Locate and identify every blood parasite.
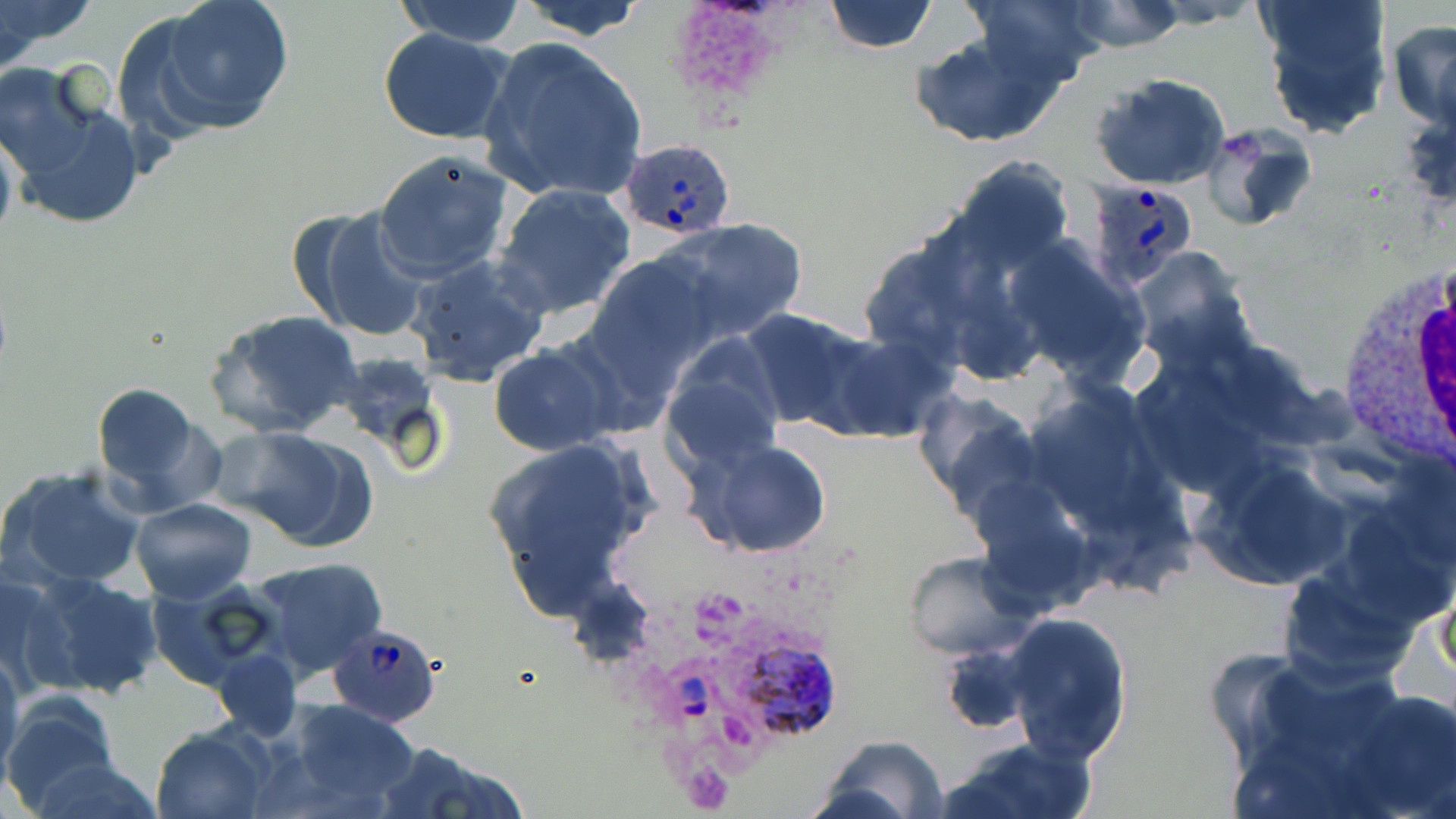

Approximate bounding boxes as named x1/y1/x2/y2 corners in pixels.
Plasmodium ovale-infected red blood cells: (x1=620, y1=135, x2=736, y2=240), (x1=1085, y1=178, x2=1198, y2=290), (x1=328, y1=622, x2=441, y2=727), (x1=660, y1=630, x2=835, y2=737).
No Plasmodium falciparum, Plasmodium malariae, Plasmodium vivax, Babesia divergens, or Trypanosoma brucei observed.

Platelet locations: (x1=664, y1=0, x2=795, y2=108). Uninfected red blood cell locations: (x1=0, y1=0, x2=99, y2=66), (x1=391, y1=0, x2=530, y2=47), (x1=513, y1=0, x2=650, y2=40), (x1=821, y1=0, x2=938, y2=54), (x1=966, y1=0, x2=1106, y2=90), (x1=1145, y1=0, x2=1262, y2=27), (x1=1256, y1=0, x2=1396, y2=139), (x1=140, y1=1, x2=296, y2=136), (x1=1065, y1=2, x2=1186, y2=52), (x1=1389, y1=17, x2=1456, y2=128), (x1=376, y1=29, x2=516, y2=145), (x1=910, y1=29, x2=1066, y2=149), (x1=477, y1=36, x2=649, y2=208), (x1=2, y1=67, x2=144, y2=228), (x1=1092, y1=71, x2=1232, y2=190), (x1=1201, y1=122, x2=1318, y2=231), (x1=0, y1=124, x2=18, y2=254), (x1=374, y1=147, x2=514, y2=282), (x1=949, y1=157, x2=1073, y2=275), (x1=490, y1=183, x2=638, y2=320), (x1=297, y1=205, x2=434, y2=344), (x1=655, y1=217, x2=807, y2=344), (x1=1004, y1=236, x2=1149, y2=383), (x1=1129, y1=245, x2=1255, y2=370), (x1=587, y1=250, x2=725, y2=381), (x1=404, y1=255, x2=550, y2=386), (x1=737, y1=307, x2=881, y2=434), (x1=204, y1=308, x2=365, y2=440), (x1=660, y1=336, x2=785, y2=475), (x1=487, y1=344, x2=623, y2=456), (x1=90, y1=381, x2=211, y2=505), (x1=1023, y1=383, x2=1169, y2=532), (x1=913, y1=390, x2=1043, y2=523), (x1=209, y1=427, x2=364, y2=544), (x1=480, y1=438, x2=656, y2=618), (x1=693, y1=439, x2=834, y2=559), (x1=1201, y1=457, x2=1350, y2=590), (x1=2, y1=464, x2=147, y2=591), (x1=130, y1=498, x2=258, y2=604), (x1=903, y1=552, x2=1029, y2=659), (x1=246, y1=557, x2=388, y2=680), (x1=0, y1=567, x2=94, y2=698), (x1=24, y1=572, x2=164, y2=699), (x1=145, y1=580, x2=285, y2=688), (x1=1432, y1=582, x2=1455, y2=678), (x1=1001, y1=613, x2=1132, y2=763), (x1=0, y1=646, x2=23, y2=784), (x1=214, y1=649, x2=300, y2=742), (x1=1221, y1=659, x2=1433, y2=819), (x1=1339, y1=687, x2=1456, y2=819), (x1=2, y1=698, x2=122, y2=812), (x1=283, y1=698, x2=421, y2=813), (x1=152, y1=726, x2=270, y2=818), (x1=820, y1=734, x2=947, y2=819), (x1=940, y1=735, x2=1095, y2=819), (x1=378, y1=742, x2=527, y2=819), (x1=25, y1=753, x2=163, y2=819). White blood cell locations: (x1=1329, y1=253, x2=1456, y2=478). Slide-level diagnosis: Plasmodium ovale. Captured at 1000x magnification. May-Grünwald-Giemsa-stained preparation. Thin blood smear. Optical microscopy. One field of a larger specimen. Image is 1456×819 pixels.